Assess the morphology of the erythrocytes.
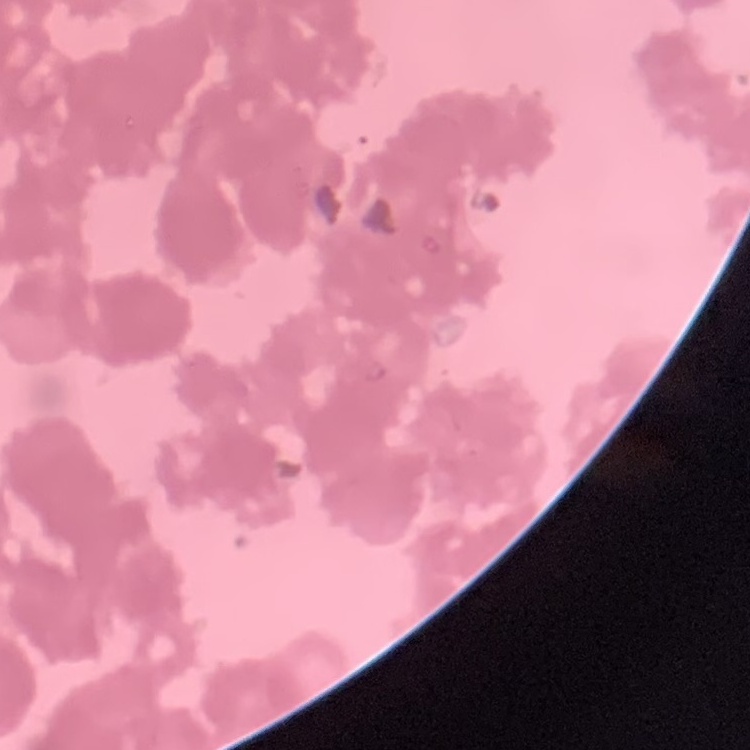

Rouleaux formation.

Square crop of a larger photomicrograph. Thin blood film. Field's or Giemsa stain.